Name the parasite shown.
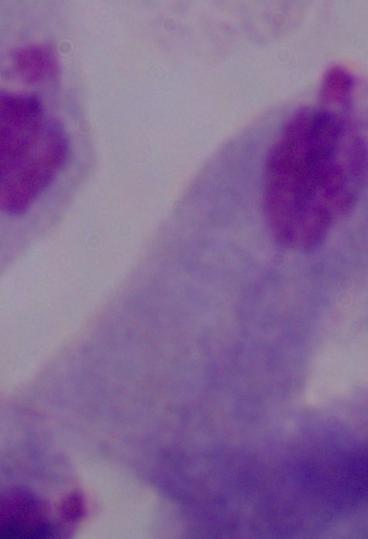

This is a trichomonad.

magnification = 1000x
modality = micrograph